Assess this cell for malaria.
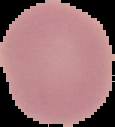
It is uninfected.

From a thin blood film. Image is 115×127 pixels. Segmented cell region on a black background.